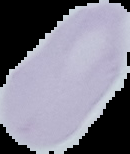

result = no malaria parasites seen
image size = 130×154 pixels
image type = cell region segmented out of the field of view; surrounding area masked to black
preparation = thin blood film